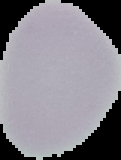

Cell region segmented out of the field of view; the surrounding area is masked to black. Result: no Plasmodium parasites detected. Image is 121×160 pixels. From a thin blood film.